Name the parasite shown.
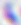

Toxoplasma gondii.

400x magnification. Micrograph.